Describe the morphology of the erythrocytes.
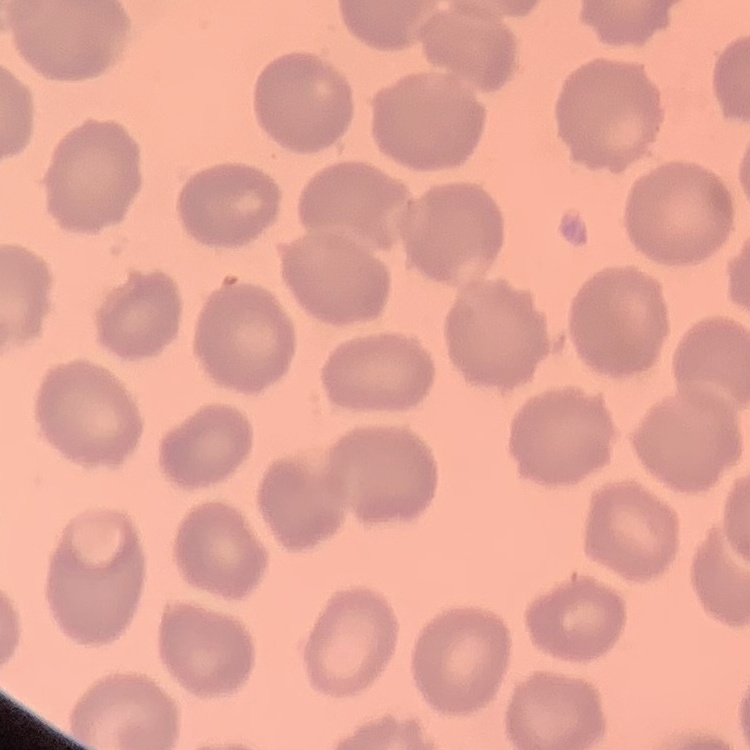

They show no rouleaux formation.

One tile cut from a larger photomicrograph. Stained with either Field's or Giemsa. Thin blood film.